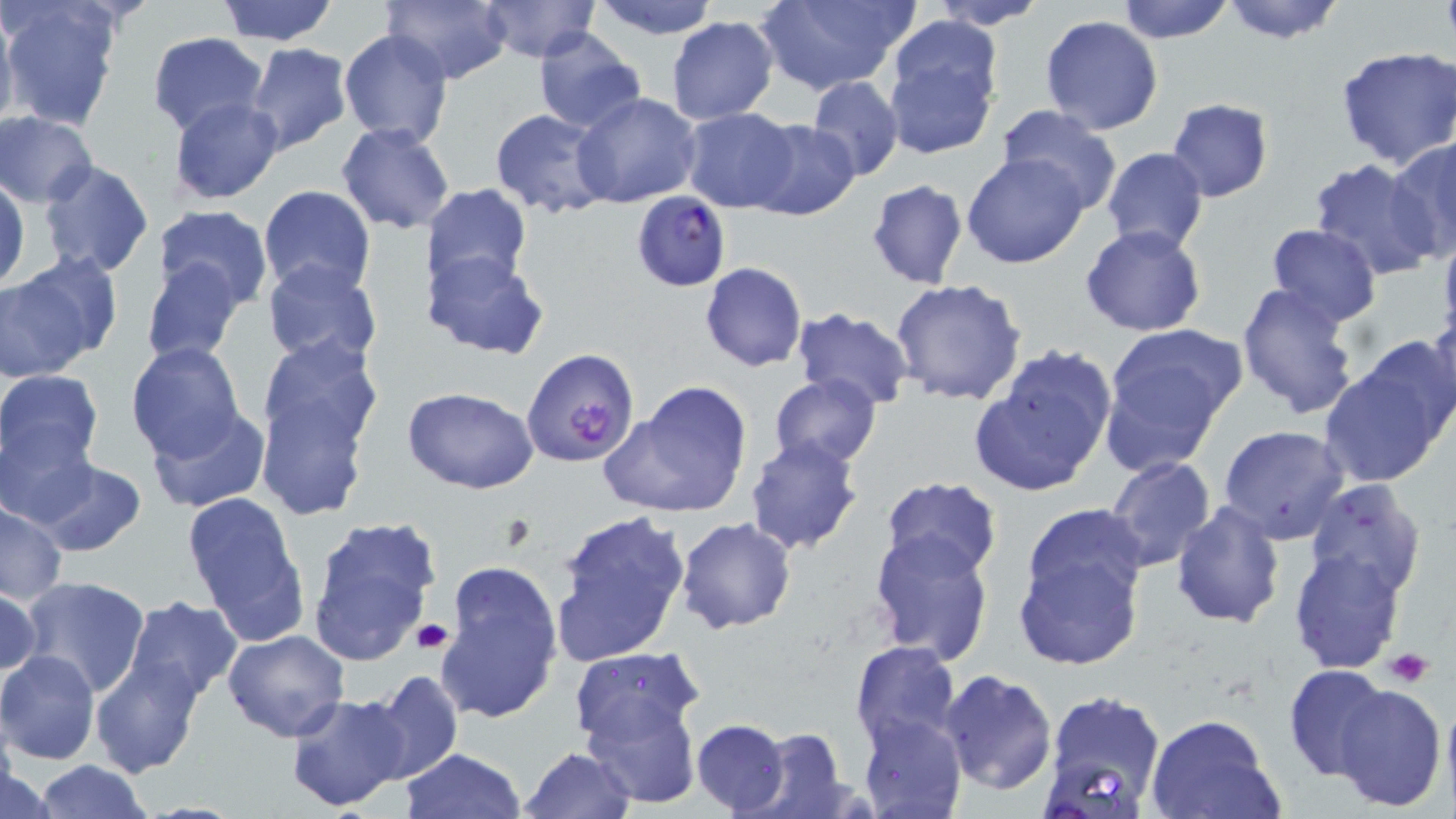
Summary:
  - Coordinate format: approximate bounding boxes as [x1, y1, x2, y2] in pixels
  - Platelet locations: [411, 619, 452, 655], [1386, 648, 1433, 687]
  - Plasmodium falciparum-infected red blood cell locations: [631, 191, 732, 291], [522, 347, 641, 468]
  - Uninfected red blood cell locations: [213, 0, 341, 46], [381, 0, 512, 86], [586, 0, 725, 41], [929, 0, 1051, 30], [1115, 0, 1237, 44], [1219, 0, 1349, 45], [477, 1, 599, 63], [750, 1, 919, 93], [2, 2, 123, 130], [0, 6, 18, 132], [1040, 15, 1163, 134], [665, 16, 779, 124], [884, 21, 1001, 159], [532, 28, 648, 134], [339, 29, 453, 149], [147, 33, 268, 136], [245, 43, 354, 156], [1335, 47, 1455, 171], [807, 76, 903, 182], [573, 92, 702, 207], [168, 97, 285, 204], [1166, 98, 1274, 202], [996, 106, 1124, 219], [679, 107, 801, 212], [490, 109, 613, 220], [1, 111, 98, 208], [745, 117, 861, 220], [336, 122, 456, 235], [1387, 137, 1456, 261], [1100, 146, 1209, 254], [961, 153, 1091, 270], [38, 158, 154, 279], [1308, 159, 1444, 281], [0, 177, 28, 293], [865, 178, 970, 291], [258, 184, 376, 296], [423, 184, 532, 299], [152, 206, 274, 310], [1264, 223, 1382, 327], [1080, 225, 1206, 337], [1437, 228, 1456, 350], [423, 247, 548, 360], [2, 254, 114, 375], [140, 256, 242, 366], [261, 259, 384, 368], [699, 262, 807, 372], [889, 278, 1028, 406], [1235, 281, 1362, 419], [791, 308, 914, 411], [1422, 315, 1456, 433], [1098, 323, 1245, 469], [252, 334, 384, 517], [125, 341, 246, 462], [968, 345, 1118, 498], [1323, 348, 1452, 486], [0, 368, 104, 477], [768, 373, 881, 469], [599, 383, 754, 520], [402, 388, 540, 494], [146, 405, 271, 514], [0, 418, 97, 525], [1218, 423, 1351, 542], [744, 434, 865, 557], [1104, 456, 1216, 573], [26, 457, 148, 558], [879, 475, 1003, 579], [1305, 478, 1429, 603], [181, 491, 310, 640], [1, 502, 69, 604], [1171, 502, 1284, 629], [549, 507, 693, 668], [1012, 508, 1149, 671], [304, 516, 440, 669], [675, 517, 797, 636], [868, 531, 996, 664], [1289, 547, 1407, 674], [435, 562, 562, 723], [18, 576, 151, 698], [0, 586, 41, 681], [121, 595, 244, 702], [222, 630, 350, 743], [850, 640, 962, 751], [569, 648, 698, 744], [0, 651, 100, 764], [89, 655, 205, 777], [1282, 663, 1397, 783], [361, 669, 463, 786], [936, 669, 1057, 793], [578, 673, 702, 803], [1327, 679, 1448, 813], [1040, 687, 1167, 813], [285, 690, 411, 814], [1441, 690, 1456, 814], [1145, 712, 1283, 819], [857, 713, 966, 819], [691, 719, 789, 814], [737, 728, 856, 818], [520, 745, 637, 819], [402, 748, 524, 819], [32, 759, 151, 819], [2, 763, 56, 818]
  - Slide-level diagnosis: Plasmodium falciparum
  - Stain: May-Grünwald-Giemsa
  - Field of view: single
  - Modality: optical microscopy
  - Image size: 1456×819 pixels
  - Magnification: 1000x
  - Preparation: thin blood film